Locate leukocytes (white blood cells).
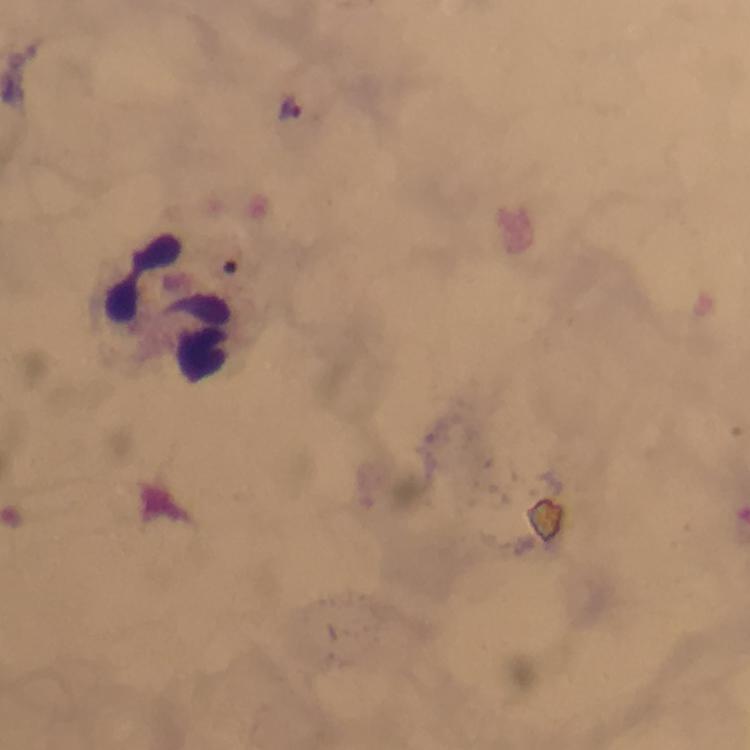

Approximate centers as {x, y} in pixels.
Leukocytes: {177, 309}.

Summary:
  - Stain: Giemsa
  - Preparation: thick blood smear
  - Cropped from: a single field of view
  - Image size: 750×750 pixels
  - Plasmodium parasites: none seen
  - Immersion oil: applied
  - Capture: smartphone camera through the microscope
  - Magnification: 100x
  - Context: from a malaria diagnostic workup